State which cell type is depicted.
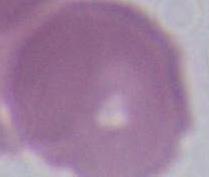
An erythrocyte.

Summary:
  - Magnification: 1000x
  - Modality: micrograph